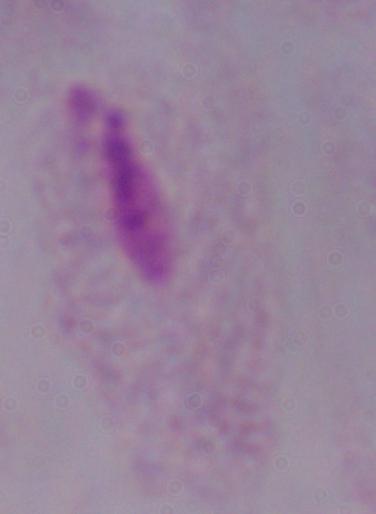

Summary:
  - Identification: trichomonad
  - Magnification: 1000x
  - Modality: photomicrograph